Assess this cell for malaria.
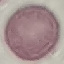

Uninfected.

Giemsa-stained preparation. Thin blood smear. Cell patch, automatically extracted from a larger field of view and resized to 64 × 64 pixels. Acquired by smartphone through the microscope eyepiece.